Assess this cell for malaria.
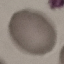
Uninfected.

Thin blood smear. Giemsa stain. Acquired by smartphone through the microscope eyepiece. Cell patch, automatically extracted from a larger field of view and resized to 64 × 64 pixels.